Assess for malaria.
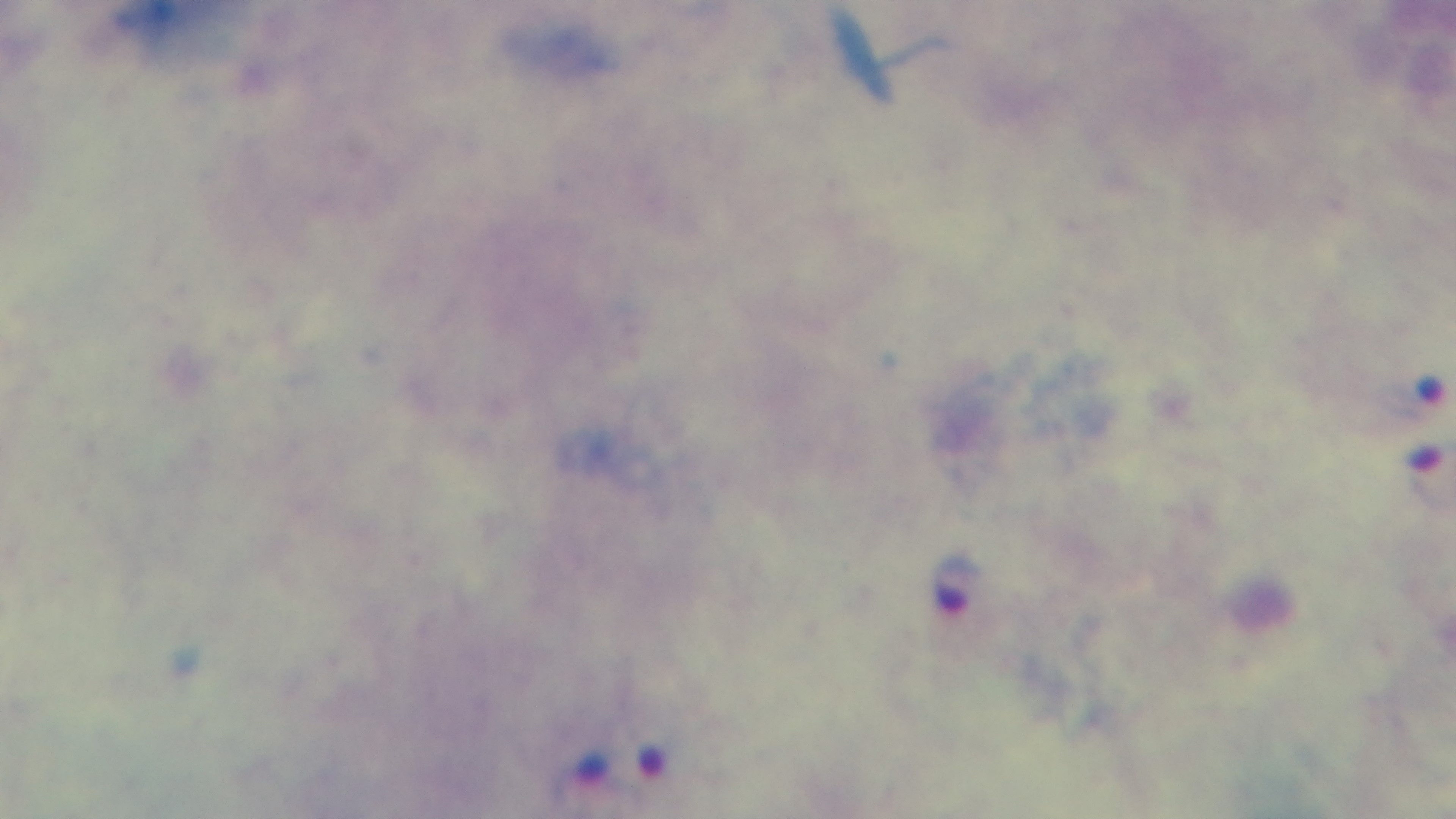

Positive.

Light microscopy. Preparation: thick blood film. 100x oil-immersion objective. Single field of view. Captured with a mounted 4K digital camera. Giemsa-stained.